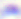

Summary:
  - Identification: Toxoplasma gondii
  - Modality: micrograph
  - Magnification: 400x